Give the position of every malaria parasite.
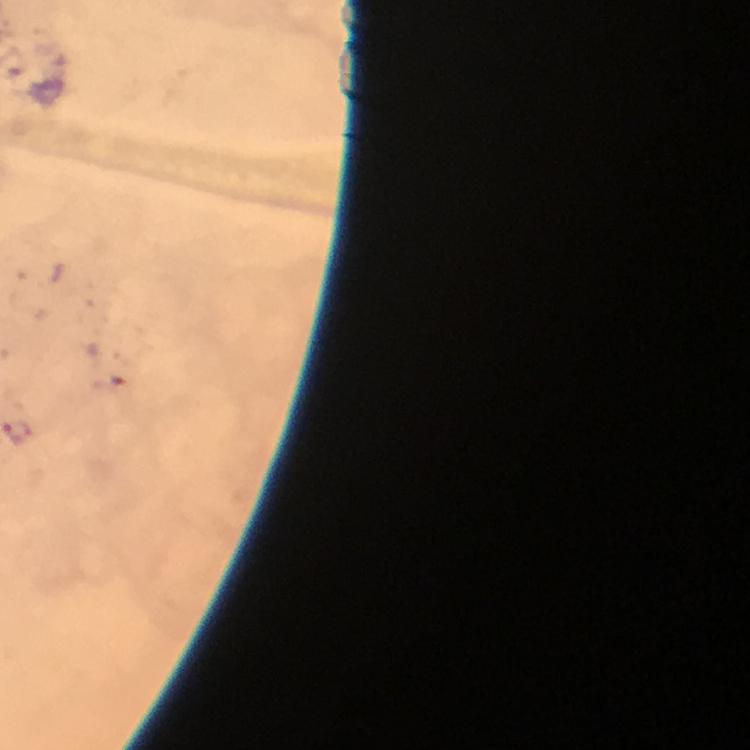
Approximate object centers, in pixels from the top-left corner.
Malaria parasites: (x=17, y=434).

Photographed through the microscope with a smartphone camera. Image is 750×750 pixels. 100x magnification. Giemsa-stained preparation. Immersion oil applied. Cropped region of a single field of view. Thick blood film. From a malaria diagnostic workup.